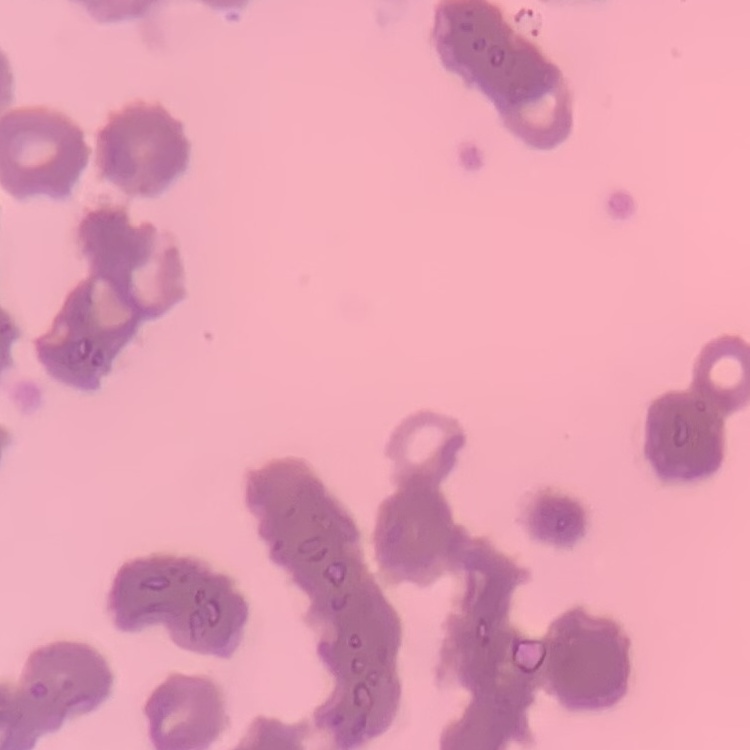

{
  "erythrocyte_morphology": "rouleaux formation",
  "preparation": "thin blood smear",
  "image_type": "one tile cut from a larger photomicrograph",
  "stain": "Field's or Giemsa"
}